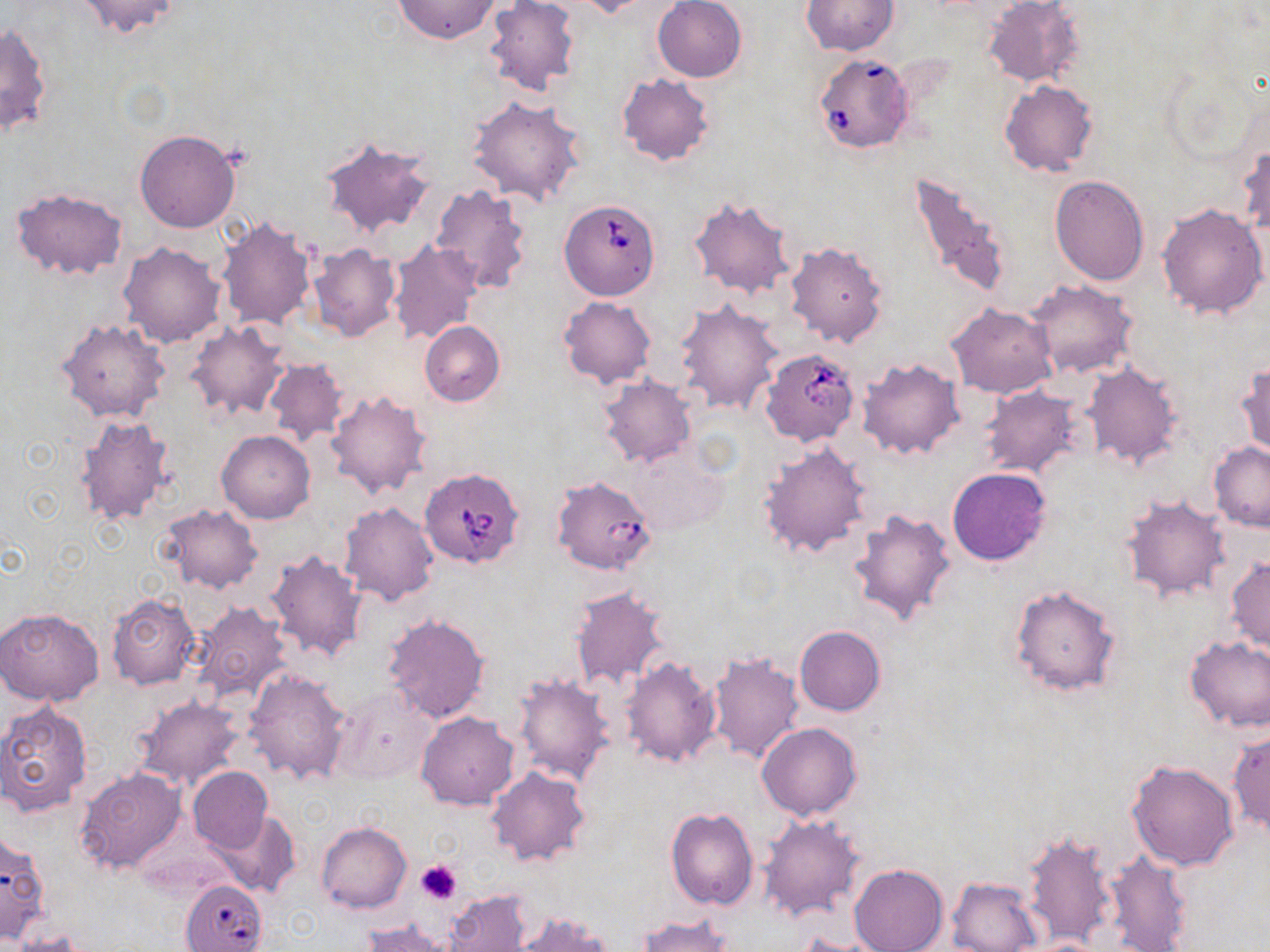

babesia_divergens_infected_red_blood_cell_locations: 'approximate bounding boxes as named x1/y1/x2/y2 corners in pixels: (x1=812, y1=52, x2=913, y2=154), (x1=559, y1=198, x2=661, y2=301), (x1=761, y1=349, x2=860, y2=447), (x1=419, y1=467, x2=526, y2=570), (x1=552, y1=474, x2=654, y2=576), (x1=181, y1=880, x2=267, y2=952)'
slide_level_diagnosis: Babesia divergens
modality: optical microscopy
image_size: 1270×952 pixels
stain: May-Grünwald-Giemsa
platelet_locations: 'approximate bounding boxes as named x1/y1/x2/y2 corners in pixels: (x1=416, y1=860, x2=463, y2=905)'
magnification: 1000x
field_of_view: single
preparation: thin blood film
uninfected_red_blood_cell_locations: 'approximate bounding boxes as named x1/y1/x2/y2 corners in pixels: (x1=74, y1=0, x2=186, y2=39), (x1=570, y1=0, x2=654, y2=19), (x1=653, y1=0, x2=747, y2=82), (x1=984, y1=0, x2=1084, y2=88), (x1=394, y1=1, x2=500, y2=44), (x1=486, y1=1, x2=580, y2=97), (x1=801, y1=1, x2=898, y2=55), (x1=0, y1=22, x2=50, y2=138), (x1=616, y1=74, x2=715, y2=166), (x1=999, y1=79, x2=1099, y2=177), (x1=468, y1=96, x2=588, y2=206), (x1=134, y1=130, x2=241, y2=233), (x1=319, y1=136, x2=438, y2=241), (x1=1238, y1=141, x2=1269, y2=242), (x1=906, y1=169, x2=1014, y2=302), (x1=1049, y1=174, x2=1151, y2=284), (x1=430, y1=183, x2=534, y2=294), (x1=10, y1=187, x2=129, y2=280), (x1=687, y1=193, x2=797, y2=300), (x1=1157, y1=202, x2=1269, y2=320), (x1=216, y1=215, x2=316, y2=332), (x1=784, y1=240, x2=889, y2=348), (x1=389, y1=241, x2=481, y2=344), (x1=119, y1=242, x2=226, y2=347), (x1=308, y1=244, x2=402, y2=343), (x1=1028, y1=280, x2=1137, y2=379), (x1=558, y1=296, x2=657, y2=390), (x1=675, y1=300, x2=782, y2=415), (x1=945, y1=302, x2=1058, y2=398), (x1=57, y1=318, x2=169, y2=424), (x1=420, y1=320, x2=505, y2=406), (x1=185, y1=322, x2=289, y2=422), (x1=856, y1=356, x2=965, y2=460), (x1=262, y1=357, x2=349, y2=448), (x1=1085, y1=361, x2=1183, y2=471), (x1=1235, y1=363, x2=1269, y2=461), (x1=598, y1=376, x2=696, y2=468), (x1=981, y1=386, x2=1082, y2=477), (x1=324, y1=387, x2=432, y2=499), (x1=71, y1=412, x2=175, y2=527), (x1=217, y1=429, x2=315, y2=523), (x1=1209, y1=441, x2=1270, y2=531), (x1=625, y1=442, x2=727, y2=538), (x1=758, y1=443, x2=873, y2=558), (x1=947, y1=466, x2=1053, y2=565), (x1=1120, y1=494, x2=1229, y2=603), (x1=339, y1=501, x2=439, y2=605), (x1=159, y1=505, x2=263, y2=593), (x1=847, y1=506, x2=956, y2=625), (x1=263, y1=549, x2=368, y2=664), (x1=1225, y1=558, x2=1270, y2=654), (x1=1009, y1=584, x2=1124, y2=698), (x1=568, y1=585, x2=671, y2=691), (x1=106, y1=592, x2=201, y2=690), (x1=190, y1=602, x2=291, y2=705), (x1=0, y1=609, x2=105, y2=705), (x1=382, y1=612, x2=490, y2=723), (x1=794, y1=625, x2=886, y2=716), (x1=1183, y1=635, x2=1270, y2=733), (x1=706, y1=652, x2=804, y2=764), (x1=620, y1=656, x2=722, y2=769), (x1=242, y1=667, x2=350, y2=786), (x1=512, y1=672, x2=614, y2=786), (x1=328, y1=683, x2=436, y2=787), (x1=132, y1=695, x2=247, y2=791), (x1=0, y1=700, x2=92, y2=816), (x1=416, y1=711, x2=519, y2=809), (x1=757, y1=723, x2=863, y2=821), (x1=1228, y1=727, x2=1269, y2=837), (x1=1126, y1=759, x2=1239, y2=871), (x1=187, y1=766, x2=272, y2=854), (x1=487, y1=766, x2=589, y2=868), (x1=74, y1=767, x2=186, y2=875), (x1=666, y1=807, x2=759, y2=911), (x1=210, y1=809, x2=300, y2=897), (x1=758, y1=814, x2=864, y2=922), (x1=316, y1=822, x2=411, y2=913), (x1=0, y1=829, x2=50, y2=943), (x1=1023, y1=829, x2=1120, y2=948), (x1=1102, y1=849, x2=1195, y2=952), (x1=850, y1=864, x2=947, y2=952), (x1=947, y1=876, x2=1043, y2=952), (x1=446, y1=889, x2=533, y2=952), (x1=513, y1=911, x2=615, y2=952), (x1=635, y1=915, x2=734, y2=952), (x1=361, y1=921, x2=457, y2=950), (x1=8, y1=933, x2=92, y2=952)'